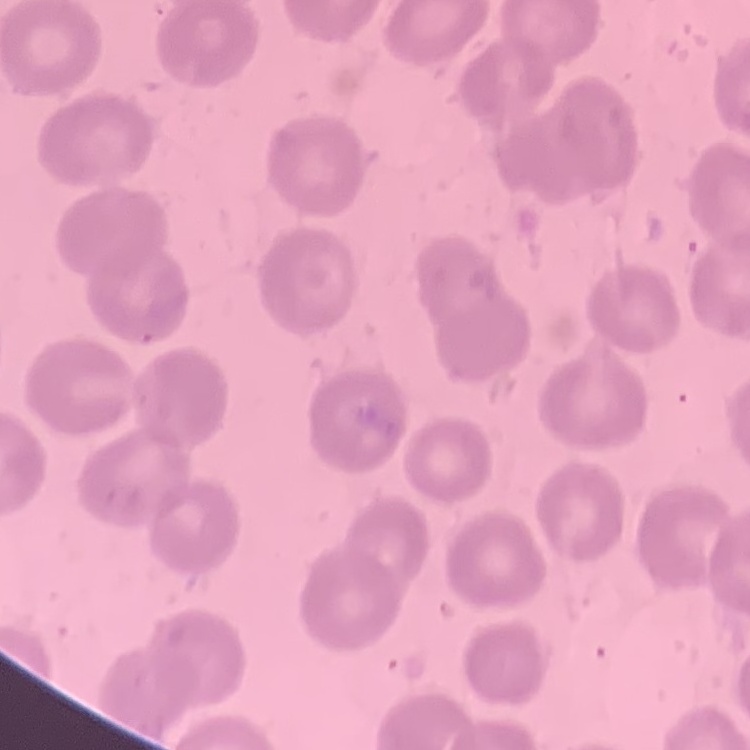
red_blood_cell_morphology: no rouleaux formation
image_type: one tile cut from a larger photomicrograph
preparation: thin peripheral smear
stain: Field's or Giemsa